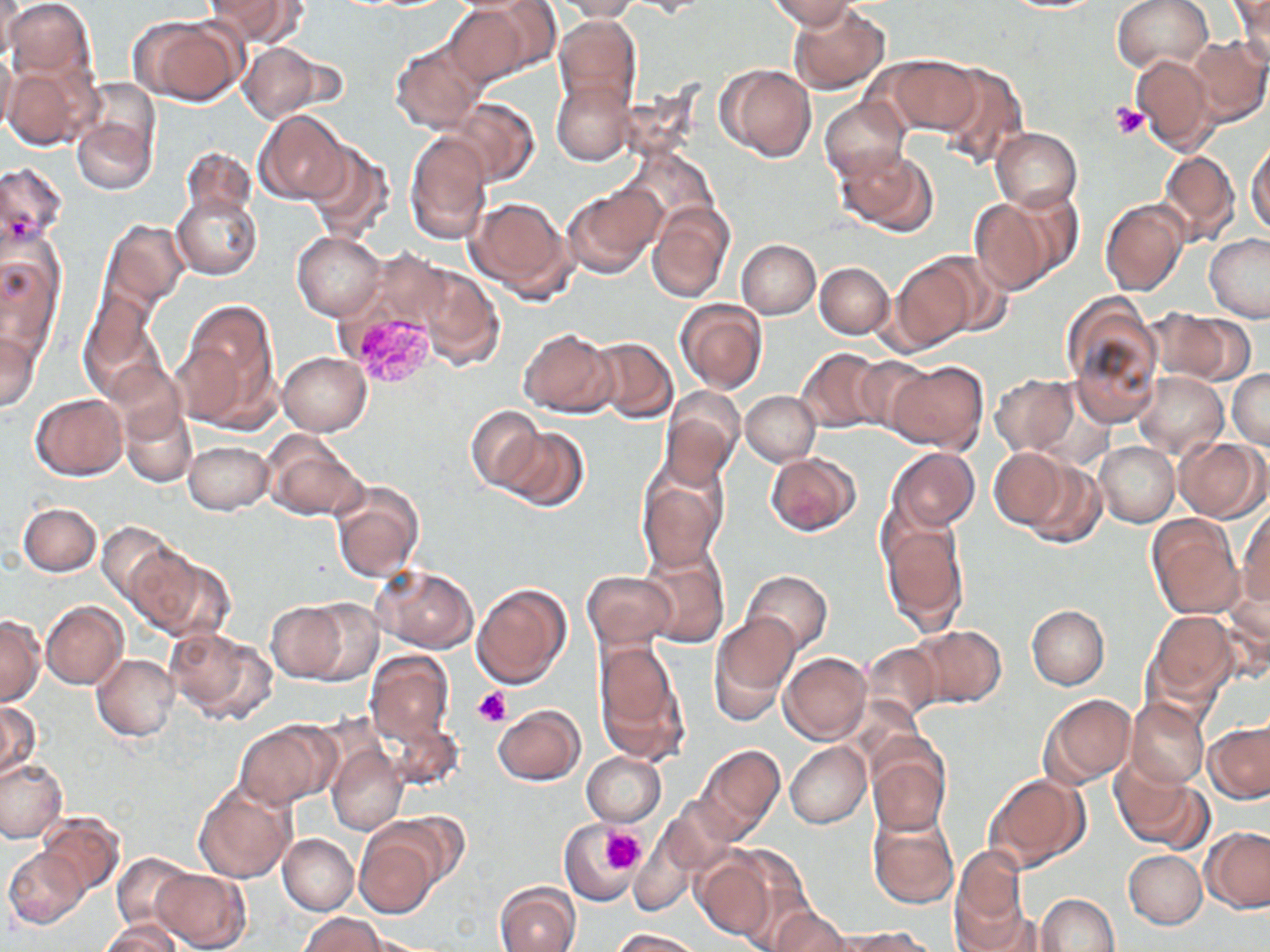
Summary:
  - Coordinate format: approximate bounding boxes as [x1, y1, x2, y2] in pixels
  - Plasmodium vivax-infected red blood cell locations: [345, 311, 439, 390]
  - Uninfected red blood cell locations: [1, 0, 95, 83], [208, 0, 305, 48], [629, 0, 708, 17], [770, 0, 856, 30], [1113, 0, 1212, 75], [1229, 0, 1270, 66], [448, 1, 548, 86], [553, 1, 639, 21], [1002, 1, 1106, 13], [789, 4, 890, 95], [554, 16, 642, 114], [138, 17, 246, 105], [1185, 36, 1269, 126], [390, 40, 487, 134], [239, 42, 326, 122], [0, 48, 17, 136], [1131, 53, 1219, 154], [880, 55, 983, 136], [3, 62, 99, 151], [931, 62, 1029, 171], [718, 64, 816, 161], [79, 78, 161, 165], [552, 81, 635, 166], [447, 97, 538, 183], [820, 97, 908, 185], [255, 111, 350, 204], [73, 114, 156, 195], [992, 128, 1081, 212], [406, 135, 491, 245], [1247, 140, 1269, 237], [304, 142, 393, 242], [620, 147, 722, 234], [181, 148, 258, 221], [834, 148, 936, 235], [1158, 149, 1240, 247], [0, 161, 67, 251], [562, 183, 665, 279], [1000, 188, 1085, 281], [172, 191, 262, 279], [467, 197, 576, 301], [969, 199, 1057, 294], [1101, 200, 1189, 297], [648, 203, 734, 306], [101, 219, 189, 311], [292, 232, 386, 320], [1204, 234, 1270, 322], [737, 240, 820, 319], [0, 245, 65, 356], [361, 246, 458, 333], [920, 250, 1010, 336], [815, 262, 893, 339], [890, 262, 973, 352], [415, 265, 503, 371], [80, 287, 164, 392], [1060, 294, 1165, 425], [675, 299, 768, 394], [178, 300, 278, 423], [1148, 309, 1253, 386], [518, 328, 616, 417], [0, 329, 40, 412], [585, 337, 678, 423], [797, 348, 887, 433], [277, 352, 371, 435], [853, 358, 933, 435], [886, 360, 987, 452], [1228, 369, 1270, 448], [1134, 371, 1228, 460], [990, 373, 1080, 455], [661, 389, 743, 489], [741, 391, 821, 466], [30, 393, 127, 480], [123, 405, 197, 486], [466, 406, 543, 490], [495, 427, 590, 513], [262, 431, 365, 520], [1172, 437, 1267, 521], [1095, 441, 1179, 526], [183, 442, 272, 514], [886, 447, 979, 533], [989, 448, 1068, 530], [765, 453, 859, 535], [1021, 460, 1105, 549], [638, 470, 726, 571], [330, 481, 424, 584], [19, 503, 100, 576], [1239, 507, 1269, 606], [1147, 516, 1245, 619], [882, 518, 968, 633], [98, 521, 179, 603], [130, 545, 233, 641], [638, 550, 729, 648], [371, 566, 477, 652], [1224, 566, 1270, 665], [742, 570, 833, 655], [582, 571, 675, 651], [474, 583, 571, 688], [300, 599, 382, 683], [263, 600, 350, 682], [41, 601, 127, 690], [1026, 605, 1109, 689], [1147, 610, 1238, 707], [709, 614, 800, 723], [0, 615, 45, 704], [909, 624, 1006, 707], [165, 626, 275, 724], [593, 642, 688, 761], [861, 642, 943, 724], [365, 651, 453, 748], [779, 652, 870, 744], [92, 654, 178, 740], [1039, 693, 1136, 788], [1126, 696, 1211, 789], [0, 701, 41, 779], [494, 704, 584, 785], [386, 719, 463, 792], [234, 722, 335, 808], [1205, 722, 1269, 804], [867, 740, 951, 836], [786, 742, 871, 828], [327, 743, 407, 836], [695, 744, 785, 841], [583, 752, 666, 826], [0, 756, 67, 843], [1112, 761, 1208, 851], [984, 774, 1089, 872], [194, 780, 295, 883], [662, 797, 740, 876], [377, 812, 470, 889], [867, 812, 958, 909], [37, 813, 124, 896], [559, 821, 639, 905], [1202, 826, 1270, 912], [354, 829, 441, 917], [629, 829, 700, 916], [278, 834, 358, 915], [4, 847, 90, 928], [1124, 850, 1207, 928], [113, 852, 194, 934], [692, 852, 775, 940], [950, 852, 1030, 949], [729, 857, 820, 948], [151, 868, 249, 951], [495, 881, 580, 952], [1037, 894, 1119, 952], [770, 907, 851, 952], [302, 914, 387, 952], [103, 919, 184, 952], [612, 928, 705, 951], [834, 928, 934, 951]
  - Platelet locations: [1112, 105, 1149, 140], [472, 688, 511, 727], [599, 826, 645, 875]
  - Slide-level diagnosis: Plasmodium vivax
  - Image size: 1270×952 pixels
  - Preparation: thin blood smear
  - Field of view: one of a larger specimen
  - Modality: light microscopy
  - Stain: May-Grünwald-Giemsa
  - Magnification: 1000x